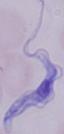

identification = trypanosome
magnification = 1000x
modality = micrograph